Report the malaria status of this cell.
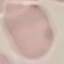

It is uninfected.

Thin smear of blood. Giemsa-stained preparation. Automatically extracted cell patch, resized to 64 × 64 pixels. Photographed with a smartphone camera at the microscope eyepiece.